Name the blood parasite species.
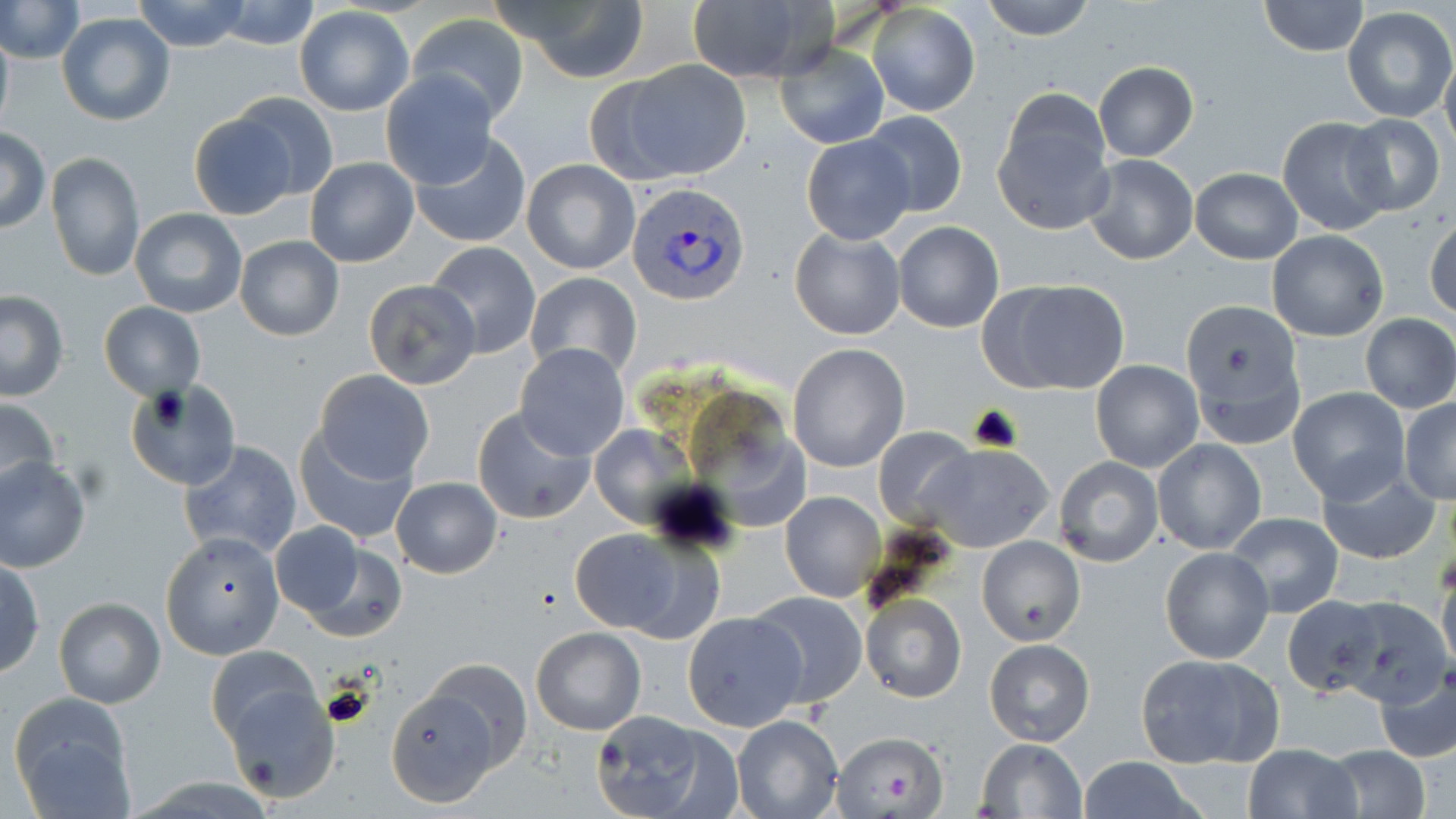

Plasmodium vivax.

{
  "image_size": "1456×819 pixels",
  "platelet_locations": "approximate bounding boxes as (x1, y1, x2, y2) in pixels: (320, 681, 376, 730)",
  "stain": "May-Grünwald-Giemsa",
  "uninfected_red_blood_cell_locations": "approximate bounding boxes as (x1, y1, x2, y2) in pixels: (0, 0, 83, 64), (132, 0, 253, 52), (490, 0, 652, 85), (980, 0, 1098, 41), (210, 1, 322, 50), (682, 1, 829, 84), (1259, 1, 1369, 55), (867, 4, 979, 117), (1343, 5, 1455, 122), (293, 7, 413, 116), (58, 12, 175, 125), (406, 14, 527, 124), (0, 23, 13, 135), (775, 40, 889, 149), (1441, 49, 1456, 156), (601, 60, 751, 182), (1092, 62, 1200, 161), (380, 71, 497, 190), (229, 92, 340, 204), (994, 92, 1114, 234), (861, 110, 968, 218), (186, 112, 298, 219), (1341, 113, 1446, 215), (1276, 116, 1392, 236), (0, 127, 50, 233), (801, 134, 915, 244), (408, 135, 532, 247), (45, 152, 146, 284), (1081, 155, 1198, 265), (304, 157, 418, 267), (522, 159, 639, 275), (1190, 167, 1302, 264), (129, 208, 248, 317), (1424, 215, 1456, 322), (894, 221, 1004, 333), (790, 227, 905, 340), (1267, 230, 1389, 341), (234, 236, 343, 342), (427, 240, 541, 357), (525, 272, 641, 379), (980, 278, 1128, 395), (363, 279, 480, 390), (0, 291, 69, 402), (98, 302, 204, 399), (1181, 306, 1304, 444), (1360, 313, 1455, 414), (514, 342, 631, 461), (787, 344, 909, 472), (1091, 359, 1205, 473), (313, 368, 435, 486), (131, 382, 238, 490), (1290, 386, 1409, 502), (0, 396, 61, 501), (1400, 397, 1456, 504), (472, 407, 596, 525), (586, 423, 692, 526), (293, 426, 419, 544), (873, 426, 976, 528), (1152, 438, 1266, 555), (179, 442, 302, 561), (919, 442, 1054, 552), (0, 456, 91, 572), (1052, 457, 1163, 568), (1314, 461, 1441, 566), (390, 476, 503, 578), (765, 492, 875, 704), (779, 492, 885, 601), (1224, 511, 1343, 620), (566, 525, 702, 635), (281, 532, 408, 643), (163, 533, 284, 658), (976, 535, 1084, 645), (1160, 546, 1274, 664), (0, 559, 46, 678), (1437, 561, 1456, 674), (749, 591, 867, 709), (861, 594, 965, 704), (1281, 596, 1385, 697), (1335, 596, 1450, 707), (54, 597, 165, 708), (682, 611, 808, 732), (530, 627, 647, 736), (984, 638, 1096, 747), (204, 645, 320, 744), (1134, 652, 1284, 770), (1372, 664, 1456, 764), (392, 673, 516, 800), (221, 685, 340, 802), (9, 695, 133, 813), (590, 711, 727, 819), (732, 715, 843, 819), (832, 729, 945, 818), (976, 738, 1088, 819), (1243, 742, 1361, 818), (1319, 746, 1432, 818), (1076, 757, 1203, 818)",
  "magnification": "1000x",
  "preparation": "thin blood film",
  "modality": "optical microscopy",
  "plasmodium_vivax_infected_red_blood_cell_locations": "approximate bounding boxes as (x1, y1, x2, y2) in pixels: (627, 181, 753, 306)",
  "field_of_view": "one of a larger specimen"
}